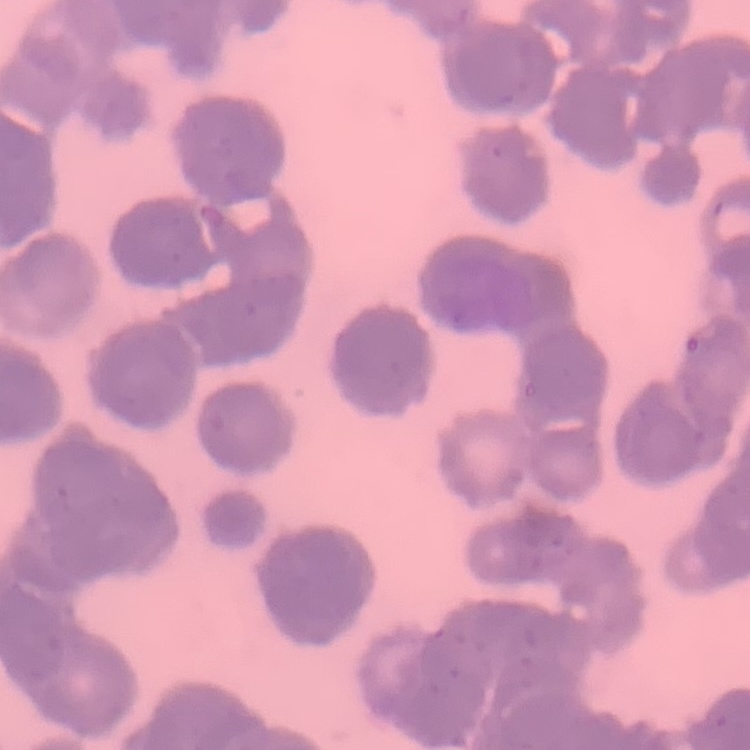

Summary:
  - Red blood cell morphology: rouleaux formation
  - Stain: Field's or Giemsa
  - Image type: one tile cut from a larger photomicrograph
  - Preparation: thin blood film